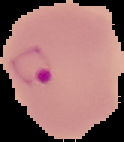
Summary:
  - Result: Plasmodium parasites detected
  - Preparation: thin blood film
  - Image type: cell region segmented out of the field of view; surrounding area masked to black
  - Image size: 124×142 pixels